State the preparation type.
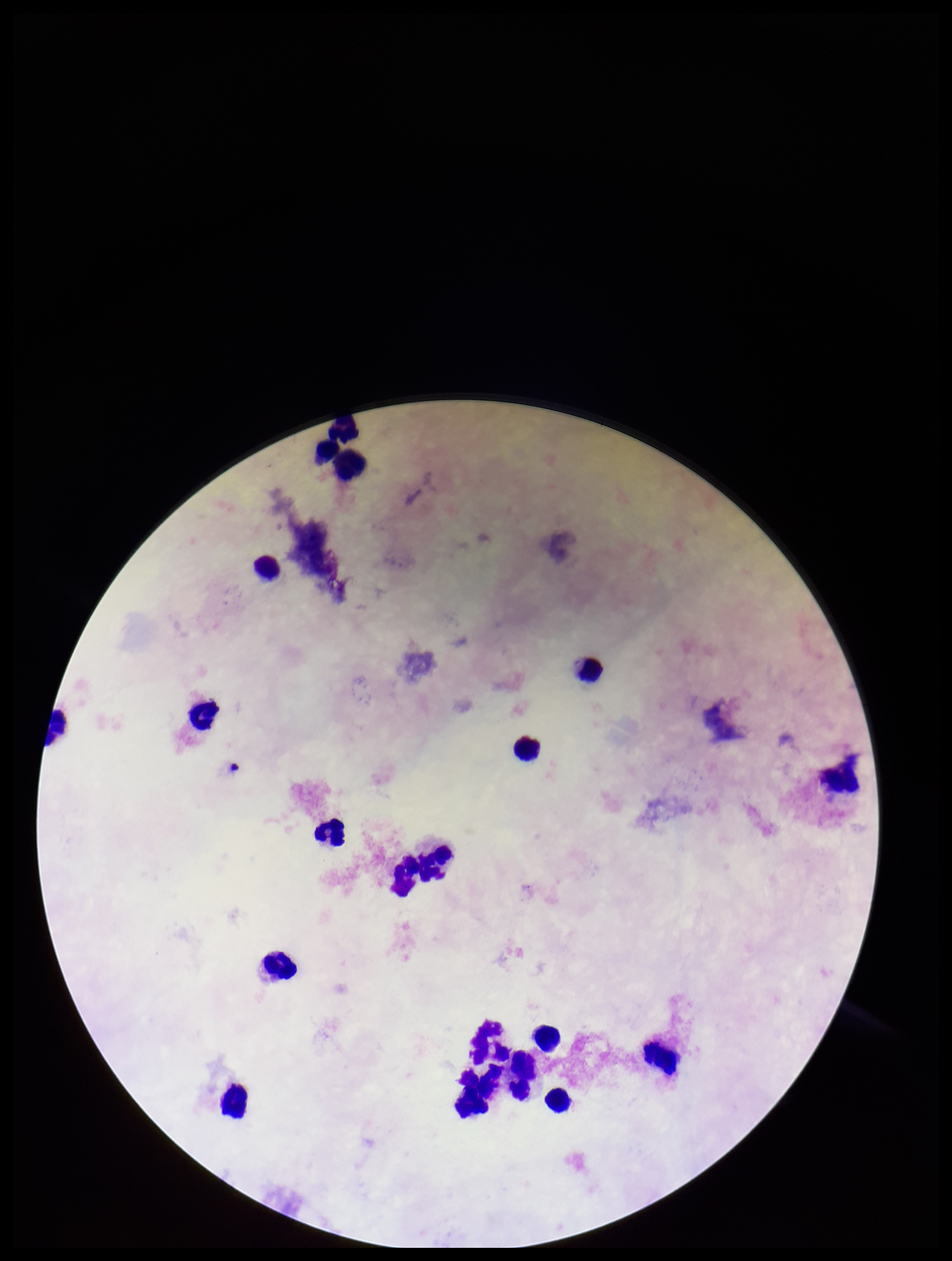
It is a thick blood smear.

Summary:
  - Parasite count: 0
  - Leukocyte count: 17
  - Patient malaria status: negative
  - Field of view: one from this slide
  - Capture: smartphone photograph through the microscope eyepiece
  - Plasmodium parasites: none detected
  - Stain: Giemsa
  - Image size: 952×1261 pixels